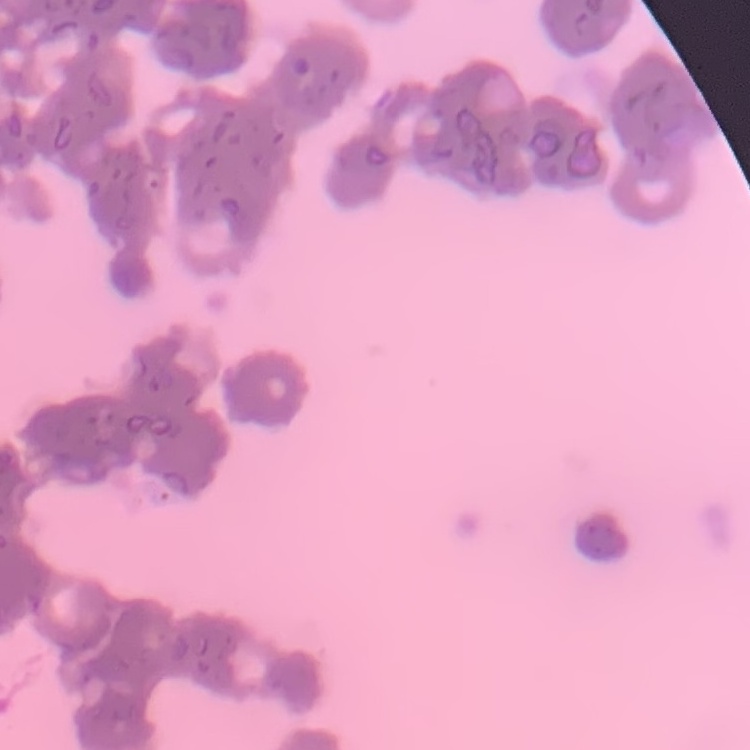

Summary:
  - Erythrocyte morphology: rouleaux formation
  - Preparation: thin blood smear
  - Image type: one tile cut from a larger photomicrograph
  - Stain: Field's or Giemsa